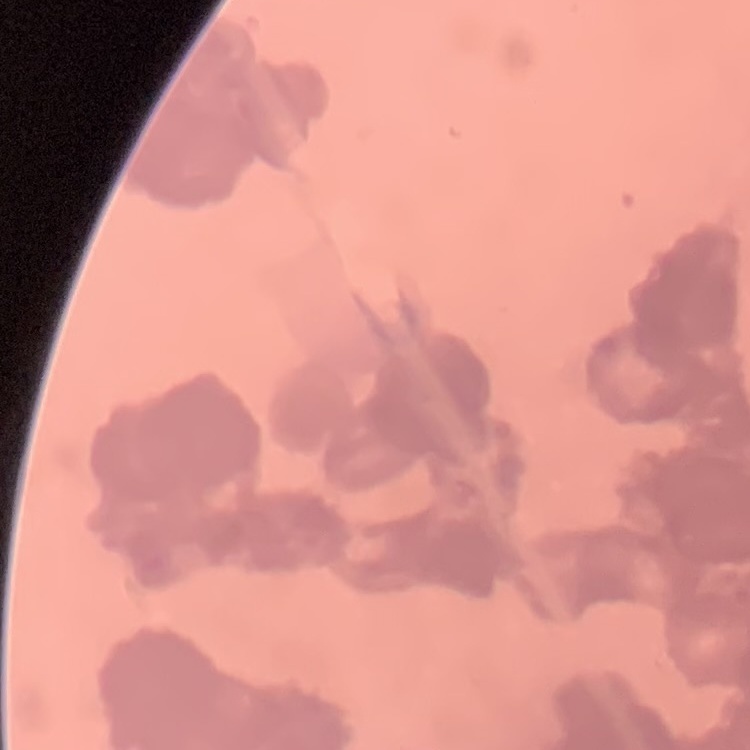
Summary:
  - Red blood cell morphology: rouleaux formation
  - Image type: one tile cut from a larger photomicrograph
  - Stain: Field's or Giemsa
  - Preparation: thin blood smear